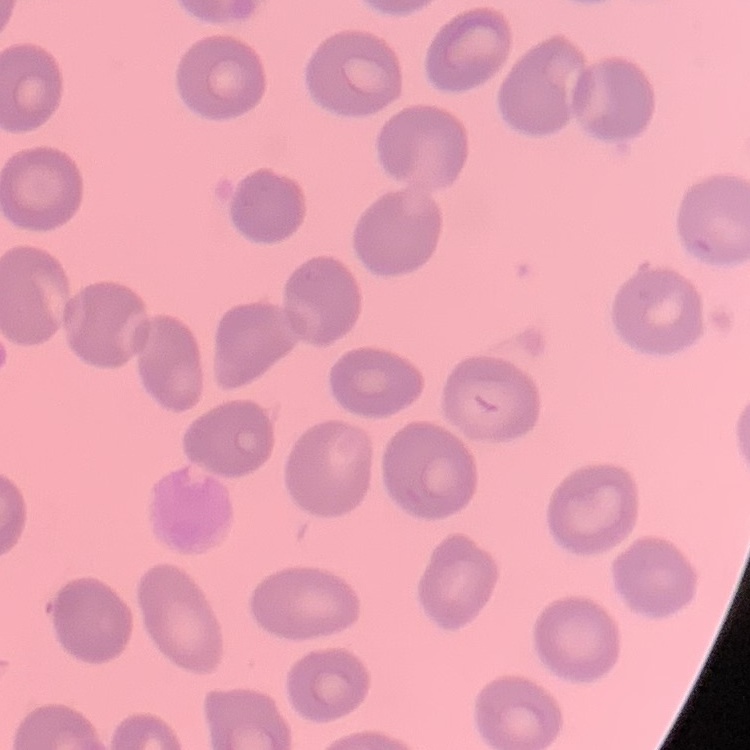

erythrocyte morphology = no rouleaux formation
image type = square crop of a larger photomicrograph
preparation = thin peripheral smear
stain = Field's or Giemsa